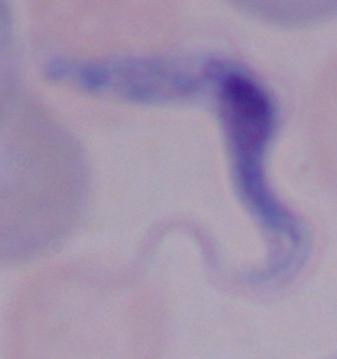

A trypanosome is shown. 1000x magnification. Photomicrograph.